Name the parasite shown.
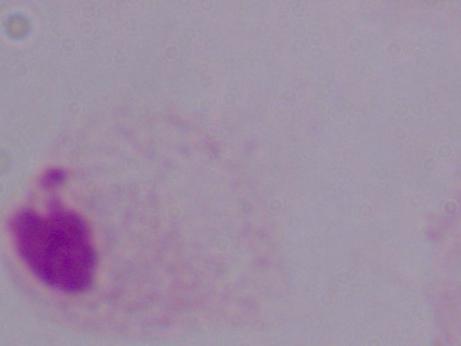

This is a trichomonad.

magnification: 1000x
modality: photomicrograph